Assess the morphology of the red blood cells.
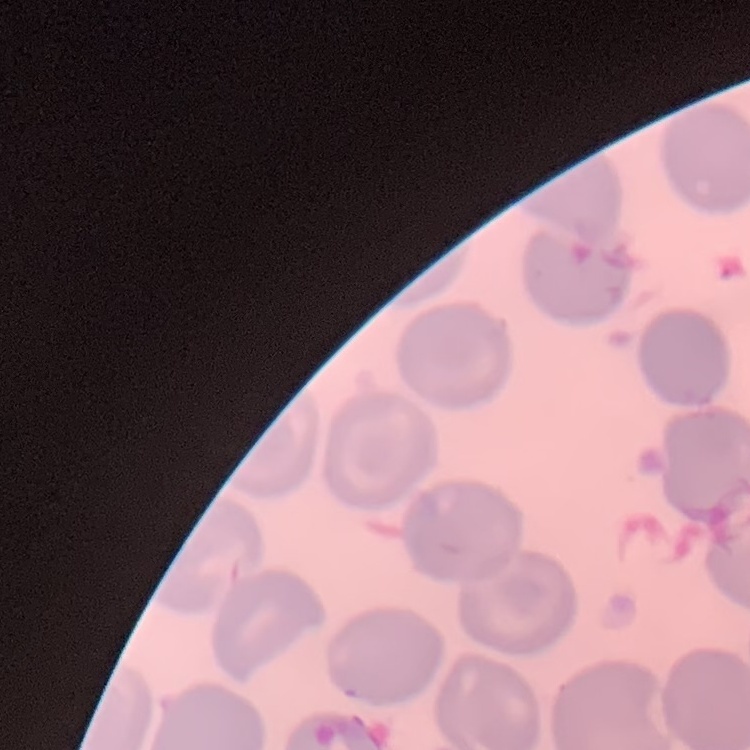

They show no rouleaux formation.

Summary:
  - Stain: Field's or Giemsa
  - Image type: square crop of a larger photomicrograph
  - Preparation: thin blood smear